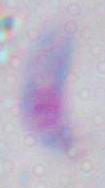

Summary:
  - Magnification: 1000x
  - Identification: Toxoplasma gondii
  - Modality: micrograph